Report the malaria status of this cell.
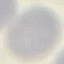
It is uninfected.

Summary:
  - Stain: Giemsa
  - Preparation: thin smear
  - Image type: cell patch, automatically extracted from a larger field of view and resized to 64 × 64 pixels
  - Capture: smartphone camera at the microscope eyepiece